Describe the morphology of the erythrocytes.
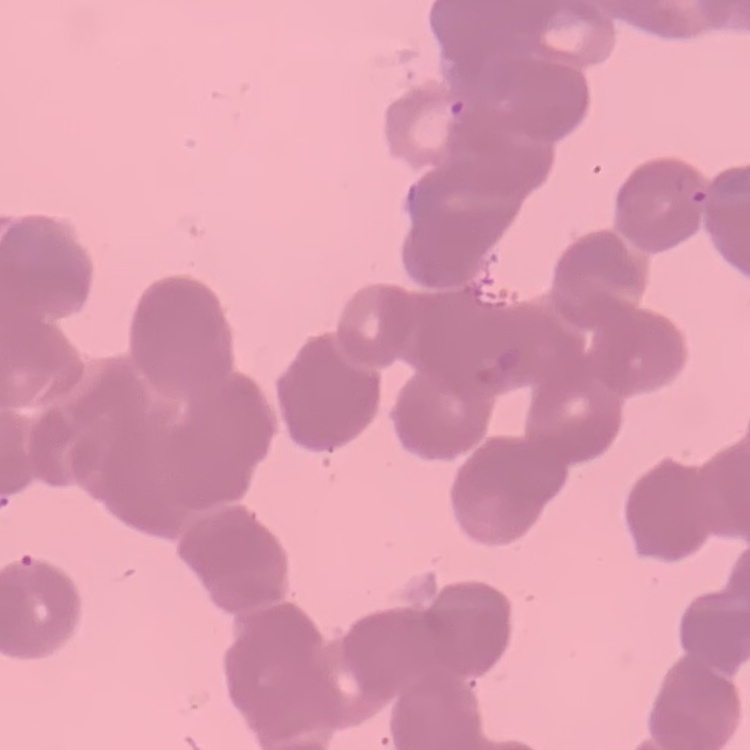

Rouleaux formation.

Summary:
  - Image type: square crop of a larger photomicrograph
  - Preparation: thin peripheral smear
  - Stain: Field's or Giemsa